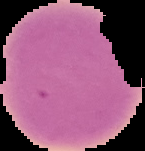
Summary:
  - Result: negative for malaria parasites
  - Image size: 145×151 pixels
  - Image type: cell region segmented out of the field of view; surrounding area masked to black
  - Preparation: thin blood smear